Give the preparation type.
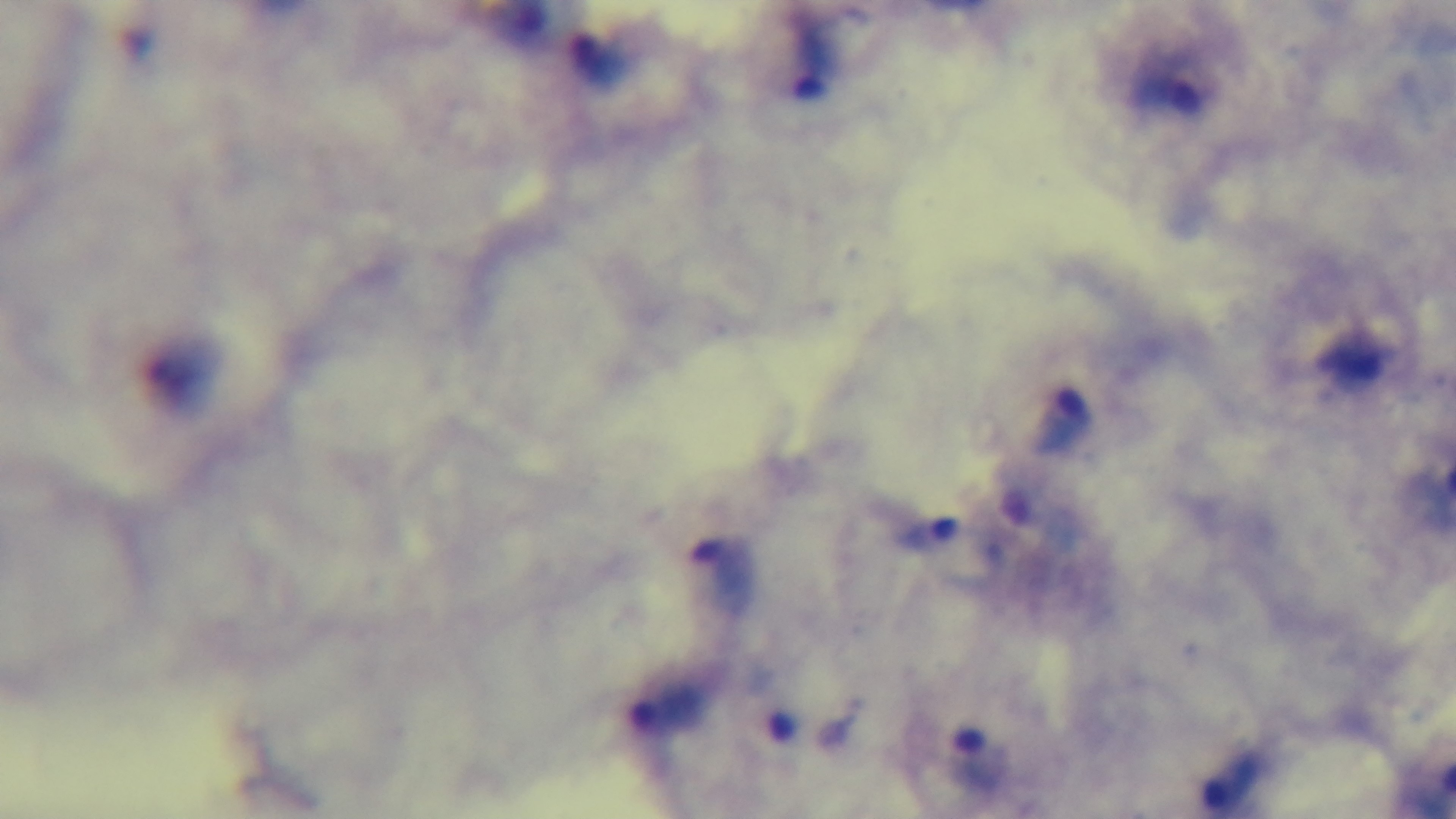
A thick smear.

malaria status = infected
modality = light microscopy
capture = mounted 4K digital camera
field of view = single
stain = Giemsa
objective = 100x oil immersion